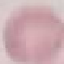

Summary:
  - Malaria status: uninfected
  - Stain: Giemsa
  - Capture: smartphone camera at the microscope eyepiece
  - Preparation: thin blood smear
  - Image type: cell patch, automatically extracted from a larger field of view and resized to 64 × 64 pixels